State which parasite is depicted.
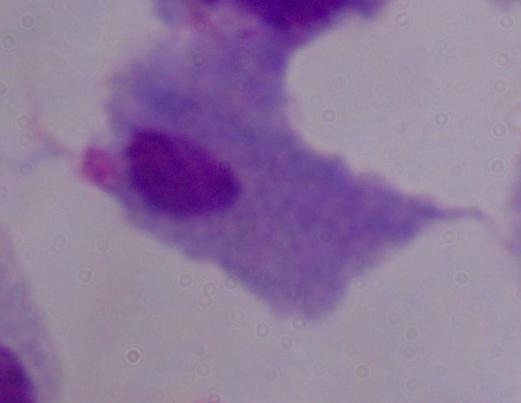

This is a trichomonad.

Captured at 1000x magnification. Photomicrograph.